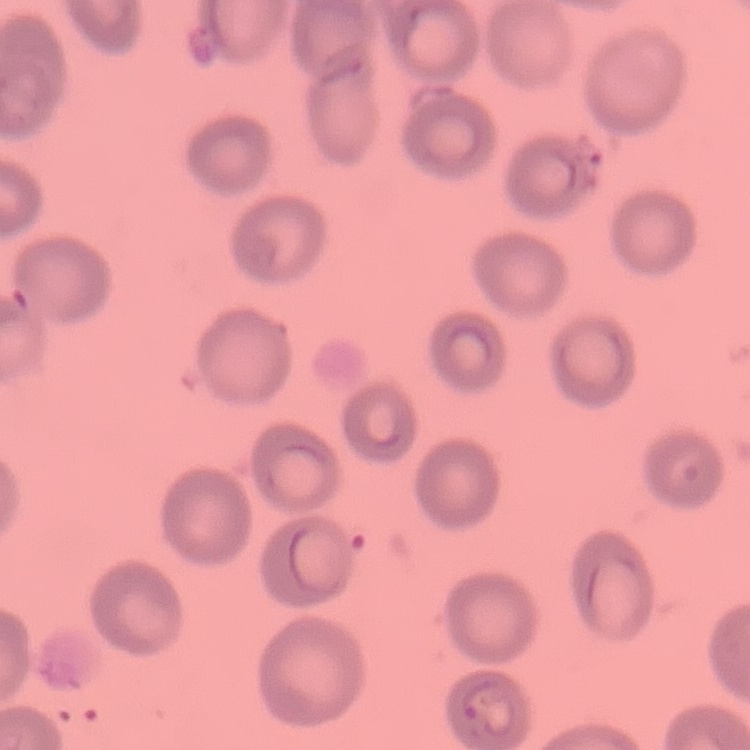
red blood cell morphology = no rouleaux formation
image type = square crop of a larger photomicrograph
stain = Field's or Giemsa
preparation = thin blood smear